Report the malaria status of this cell.
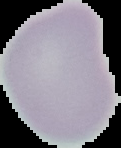
Uninfected.

Image is 121×148 pixels. From a thin blood smear. Cell region segmented out of the field of view; the surrounding area is masked to black.